Point out every Plasmodium parasite and every leukocyte.
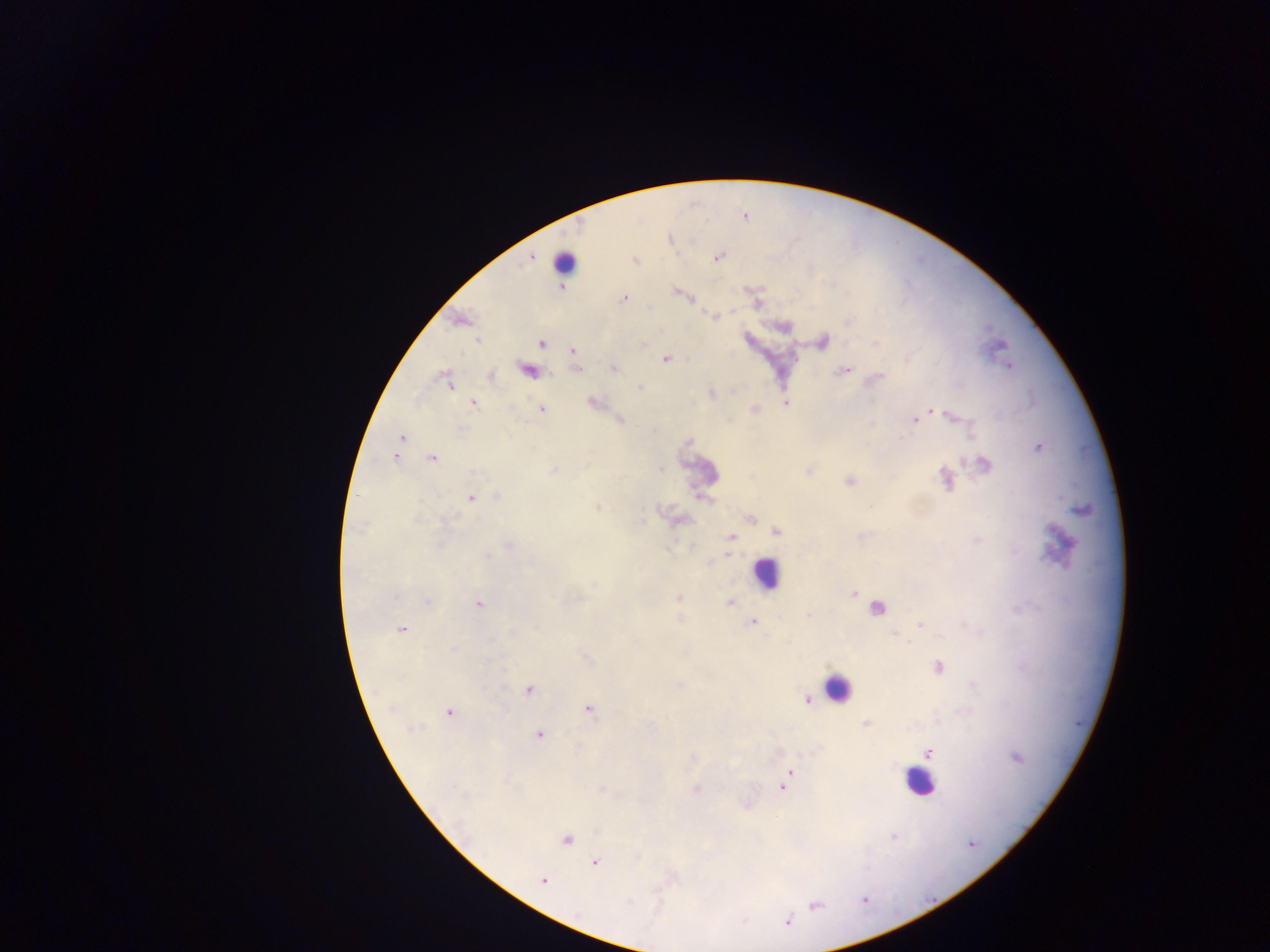
Approximate centers as x y in pixels.
Plasmodium parasites: 531 256; 716 256; 635 260; 560 288; 678 292; 623 298; 715 315; 460 320; 479 339; 823 341; 541 342; 573 351; 665 358; 1009 366; 575 368; 613 368; 527 369; 843 370; 489 375; 875 379; 448 384; 639 387; 710 392; 473 402; 592 402; 786 402; 541 408; 754 409; 931 409; 618 419; 914 419; 401 437; 397 447; 1038 447; 395 456; 433 458; 983 464; 554 469; 945 478; 850 480; 471 497; 497 497; 598 508; 750 518; 776 531; 731 536; 508 546; 728 552; 852 593; 678 597; 729 602; 478 605; 875 608; 752 622; 920 624; 401 629; 937 667; 528 689; 806 700; 588 708; 449 712; 867 723; 538 734; 927 753; 1015 756; 692 758; 788 772; 786 780; 602 787; 781 788; 694 789; 746 804; 566 839; 594 862; 542 880.
Leukocytes: 564 261; 699 471; 1062 544; 765 574; 836 687; 920 782.

capture: mobile-phone photograph through a microscope
preparation: thick blood smear
country: Ghana
image_size: 1270×952 pixels
field_of_view: single